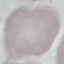

Summary:
  - Malaria status: uninfected
  - Image type: cell patch, automatically extracted from a larger field of view and resized to 64 × 64 pixels
  - Stain: Giemsa
  - Preparation: thin blood film
  - Capture: smartphone camera at the microscope eyepiece